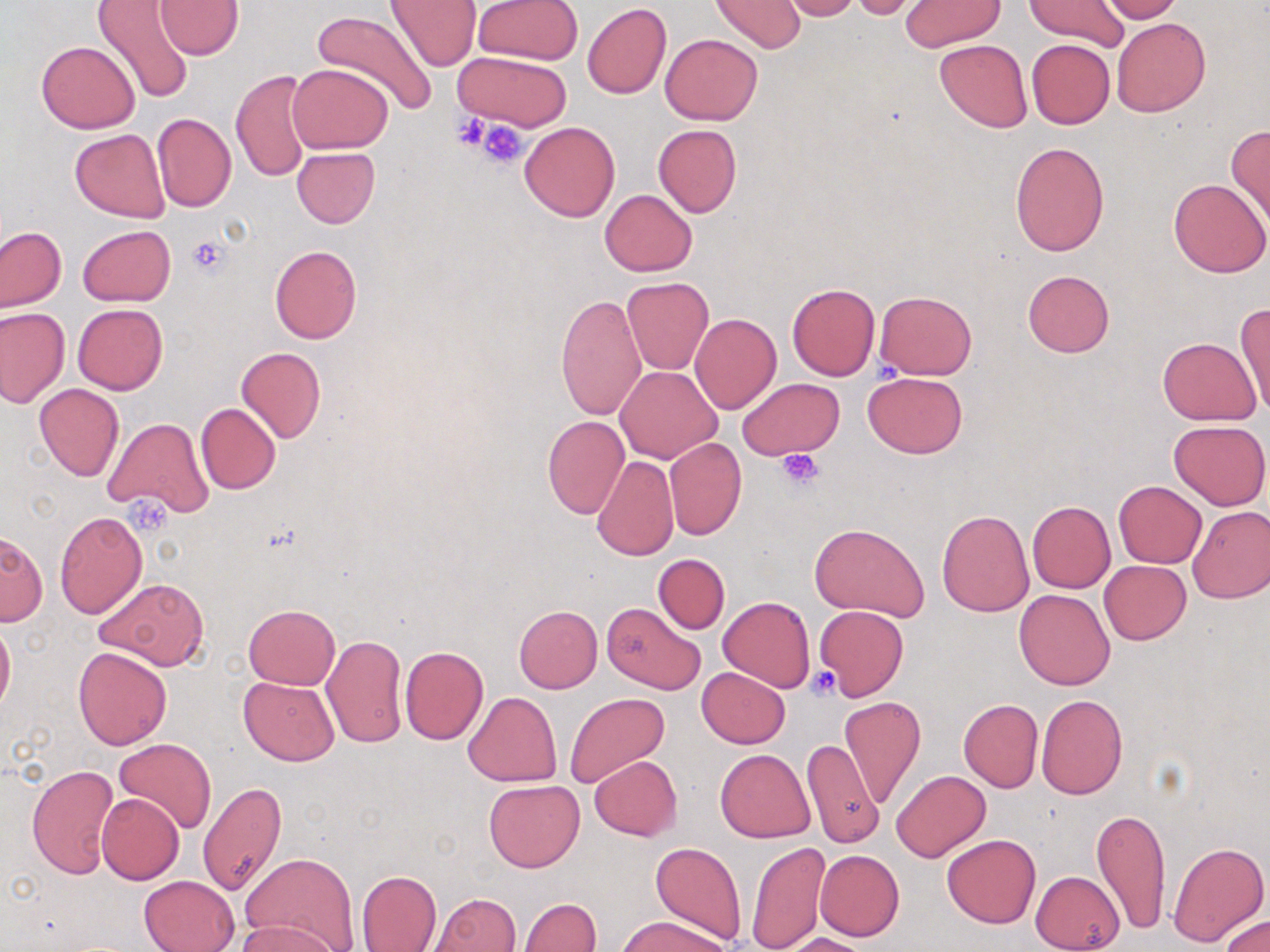

Summary:
  - Coordinate format: approximate bounding boxes as (x1,y1)-(x2,y2) corner pairs in pixels
  - Platelet locations: (452,112)-(493,152), (475,120)-(531,168), (187,234)-(231,278), (777,450)-(824,491), (805,666)-(841,699)
  - Uninfected red blood cell locations: (385,0)-(482,71), (475,0)-(583,65), (1024,0)-(1130,50), (1095,0)-(1182,22), (155,1)-(243,59), (712,1)-(804,52), (777,1)-(862,21), (848,1)-(924,21), (900,1)-(1005,50), (91,2)-(194,104), (582,4)-(672,100), (313,10)-(440,116), (1113,19)-(1210,116), (661,34)-(763,125), (934,39)-(1032,132), (1025,39)-(1115,129), (36,40)-(140,133), (452,50)-(574,132), (288,63)-(393,152), (232,69)-(314,182), (152,113)-(236,211), (520,121)-(620,221), (653,124)-(742,216), (1226,125)-(1270,229), (70,128)-(169,221), (1009,141)-(1109,256), (292,147)-(380,228), (1168,177)-(1269,277), (599,189)-(697,276), (78,224)-(175,306), (0,226)-(66,311), (269,245)-(362,344), (1022,269)-(1114,357), (623,277)-(714,374), (787,283)-(879,381), (875,291)-(977,379), (555,294)-(647,421), (73,303)-(168,394), (1234,304)-(1270,413), (1,308)-(69,407), (689,314)-(781,414), (1158,337)-(1260,424), (236,346)-(327,443), (615,365)-(723,463), (862,372)-(968,458), (737,377)-(843,460), (34,383)-(123,481), (196,403)-(281,494), (542,416)-(629,518), (104,417)-(212,518), (1171,419)-(1269,509), (665,438)-(747,540), (592,455)-(679,560), (1114,481)-(1206,567), (1027,501)-(1115,593), (1187,504)-(1270,603), (938,509)-(1035,618), (54,512)-(147,618), (809,523)-(928,620), (0,533)-(46,626), (653,553)-(730,634), (1100,560)-(1191,643), (95,577)-(208,669), (1014,588)-(1116,689), (719,596)-(814,693), (244,603)-(339,689), (603,604)-(704,695), (514,605)-(602,693), (815,606)-(908,701), (0,618)-(15,713), (322,634)-(408,748), (399,646)-(488,744), (72,647)-(172,750), (697,668)-(790,748), (238,677)-(338,766), (464,692)-(561,787), (564,692)-(668,790), (1035,694)-(1128,798), (839,696)-(927,808), (958,699)-(1043,792), (801,737)-(883,848), (114,738)-(217,835), (715,749)-(815,843), (142,752)-(250,882), (589,756)-(682,841), (25,764)-(119,879), (891,769)-(991,863), (484,780)-(585,872), (198,781)-(286,898), (97,794)-(184,884), (1091,807)-(1171,935), (941,834)-(1040,928), (1167,840)-(1268,947), (746,841)-(830,952), (650,842)-(747,946), (815,850)-(905,941), (243,852)-(357,950), (1030,870)-(1124,952), (356,871)-(441,952), (138,875)-(240,952), (427,893)-(522,952), (519,898)-(600,952), (620,914)-(730,952), (1218,915)-(1270,952), (236,918)-(337,952), (780,933)-(873,952)
  - Slide-level diagnosis: no evidence of blood parasites
  - Preparation: thin blood film
  - Field of view: one of a larger specimen
  - Stain: May-Grünwald-Giemsa
  - Image size: 1270×952 pixels
  - Modality: optical microscopy
  - Magnification: 1000x